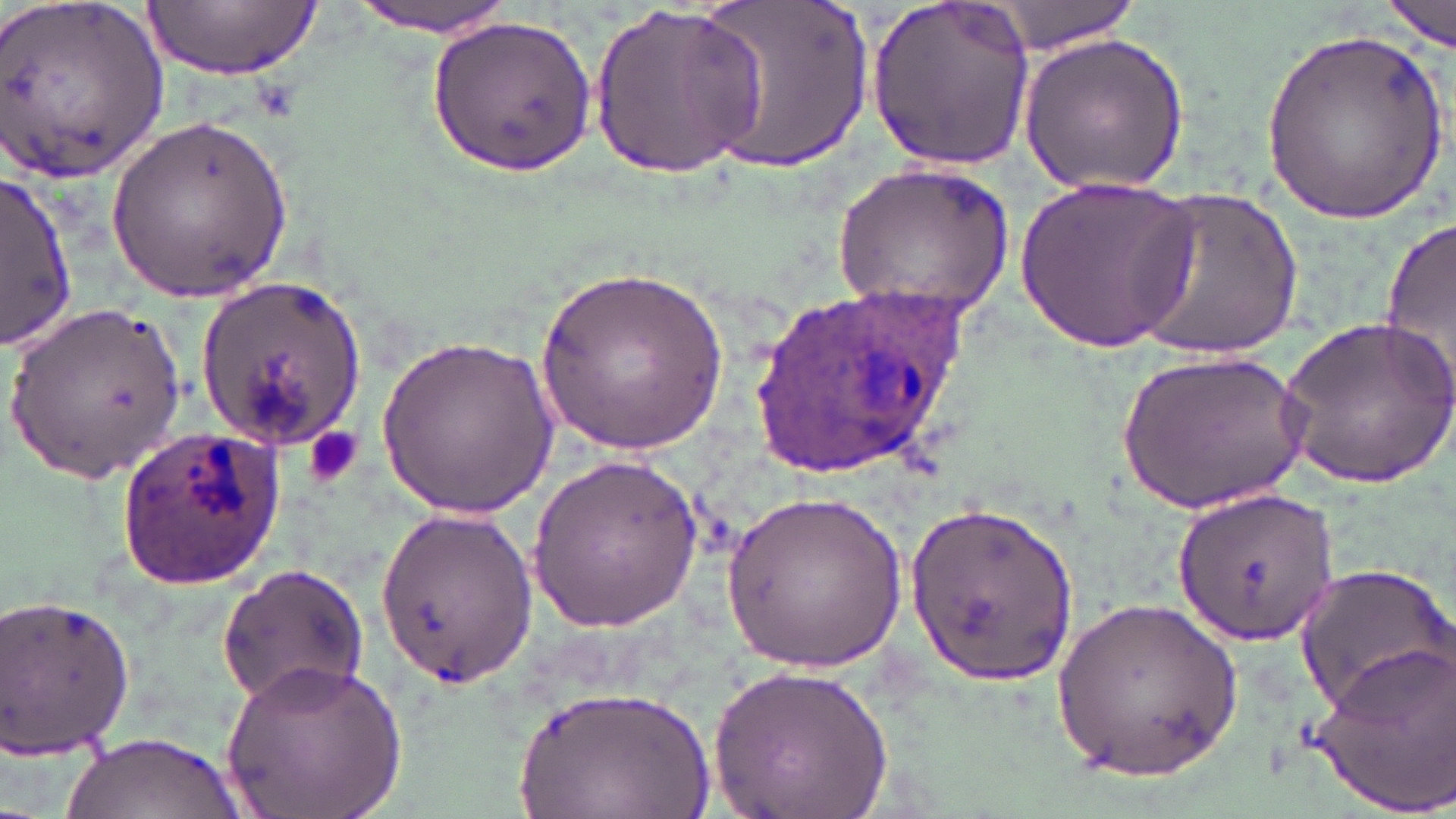

{
  "slide_level_diagnosis": "Plasmodium ovale",
  "magnification": "1000x",
  "platelet_locations": "approximate bounding boxes as named x1/y1/x2/y2 corners in pixels: (x1=304, y1=427, x2=363, y2=487)",
  "preparation": "thin blood smear",
  "uninfected_red_blood_cell_locations": "approximate bounding boxes as named x1/y1/x2/y2 corners in pixels: (x1=0, y1=0, x2=168, y2=183), (x1=145, y1=0, x2=318, y2=83), (x1=344, y1=0, x2=523, y2=35), (x1=689, y1=0, x2=874, y2=174), (x1=865, y1=0, x2=1040, y2=167), (x1=1384, y1=0, x2=1454, y2=51), (x1=977, y1=1, x2=1150, y2=55), (x1=589, y1=2, x2=769, y2=177), (x1=428, y1=14, x2=597, y2=176), (x1=1262, y1=26, x2=1446, y2=229), (x1=1018, y1=28, x2=1193, y2=195), (x1=104, y1=112, x2=294, y2=307), (x1=833, y1=162, x2=1015, y2=321), (x1=0, y1=171, x2=79, y2=350), (x1=1015, y1=174, x2=1198, y2=351), (x1=1132, y1=185, x2=1304, y2=358), (x1=1380, y1=214, x2=1456, y2=399), (x1=537, y1=263, x2=730, y2=456), (x1=194, y1=274, x2=367, y2=454), (x1=4, y1=302, x2=189, y2=487), (x1=1277, y1=314, x2=1456, y2=487), (x1=375, y1=332, x2=559, y2=520), (x1=1121, y1=348, x2=1308, y2=517), (x1=526, y1=455, x2=707, y2=629), (x1=1173, y1=485, x2=1339, y2=648), (x1=724, y1=490, x2=913, y2=672), (x1=907, y1=496, x2=1079, y2=681), (x1=373, y1=501, x2=536, y2=685), (x1=1292, y1=560, x2=1456, y2=718), (x1=217, y1=563, x2=369, y2=705), (x1=0, y1=588, x2=138, y2=767), (x1=1051, y1=593, x2=1243, y2=787), (x1=1308, y1=638, x2=1456, y2=817), (x1=219, y1=656, x2=409, y2=819), (x1=708, y1=663, x2=893, y2=819), (x1=512, y1=686, x2=716, y2=819), (x1=61, y1=730, x2=239, y2=819)",
  "stain": "May-Grünwald-Giemsa",
  "plasmodium_ovale_infected_red_blood_cell_locations": "approximate bounding boxes as named x1/y1/x2/y2 corners in pixels: (x1=744, y1=280, x2=973, y2=484), (x1=117, y1=425, x2=289, y2=590)",
  "image_size": "1456×819 pixels",
  "modality": "light microscopy",
  "field_of_view": "single"
}